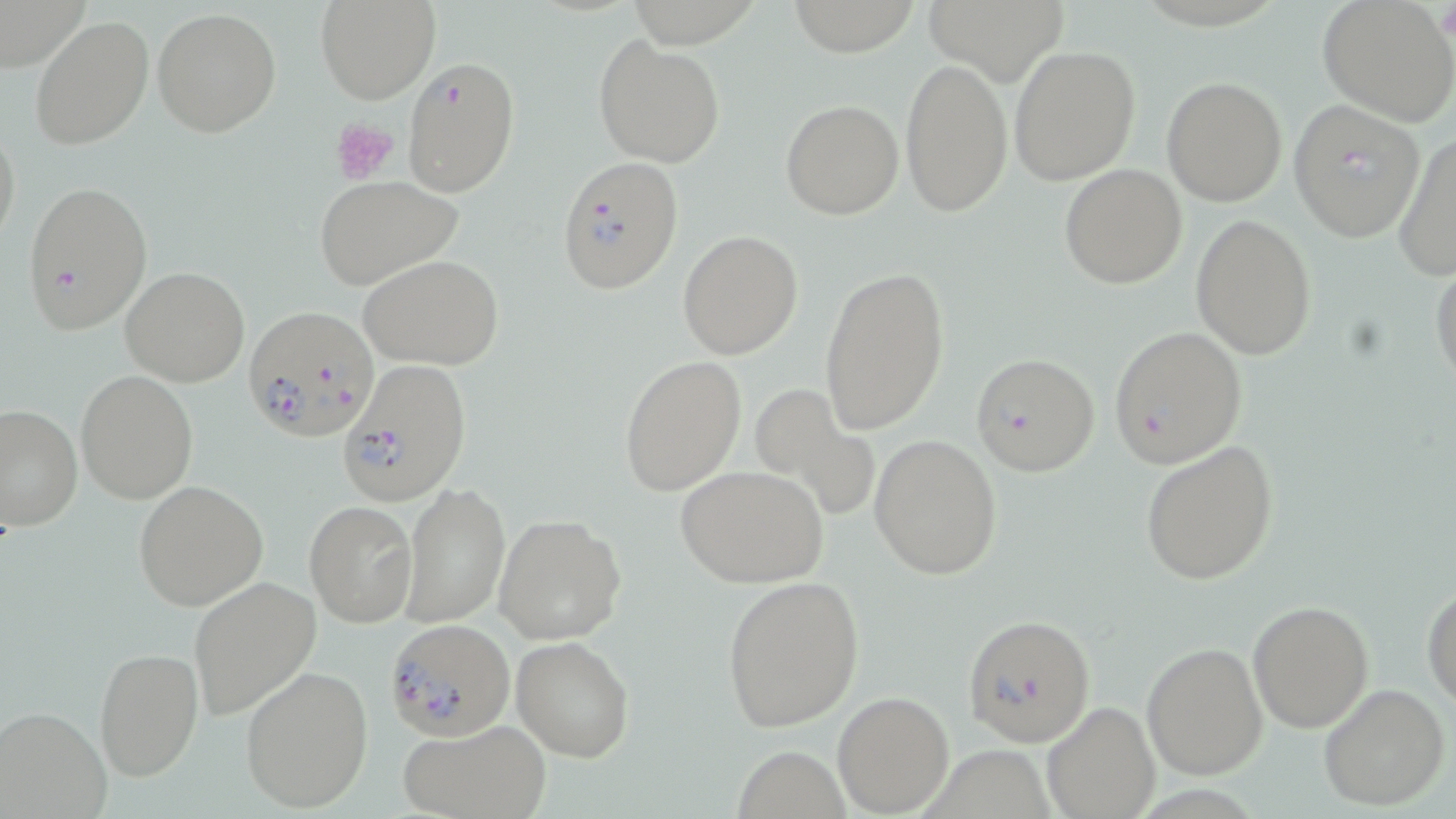
slide-level diagnosis = Plasmodium falciparum
image size = 1456×819 pixels
stain = May-Grünwald-Giemsa
modality = optical microscopy
magnification = 1000x
uninfected red blood cell locations = approximate bounding boxes as (x1,y1)-(x2,y2) corner pairs in pixels: (316,0)-(438,103), (785,0)-(924,56), (1317,1)-(1455,125), (151,7)-(281,139), (29,14)-(154,150), (594,35)-(725,167), (1008,45)-(1141,186), (900,57)-(1013,218), (1161,77)-(1288,206), (780,99)-(904,220), (0,121)-(21,253), (1392,129)-(1456,282), (1059,163)-(1187,289), (314,176)-(462,291), (1191,215)-(1316,361), (677,231)-(802,359), (359,254)-(504,370), (1430,259)-(1456,396), (819,265)-(951,435), (120,267)-(251,387), (620,355)-(746,496), (75,370)-(198,504), (748,383)-(878,523), (0,404)-(82,532), (869,434)-(1002,581), (1138,439)-(1280,585), (677,465)-(829,588), (134,480)-(269,611), (402,482)-(510,626), (304,500)-(417,627), (494,515)-(625,645), (188,574)-(322,723), (720,574)-(865,732), (1423,583)-(1456,710), (1247,599)-(1374,730), (512,635)-(635,760), (1141,641)-(1269,779), (93,645)-(204,782), (240,664)-(373,813), (1318,683)-(1449,811), (832,691)-(955,817), (1042,700)-(1159,819), (0,705)-(112,817), (397,720)-(551,819), (735,742)-(852,817)
platelet locations = approximate bounding boxes as (x1,y1)-(x2,y2) corner pairs in pixels: (1436,6)-(1456,43), (332,117)-(399,187)
Plasmodium falciparum-infected red blood cell locations = approximate bounding boxes as (x1,y1)-(x2,y2) corner pairs in pixels: (402,57)-(520,196), (1288,100)-(1428,240), (554,154)-(684,294), (22,179)-(153,335), (242,305)-(376,441), (1109,326)-(1248,470), (972,353)-(1100,477), (337,358)-(472,508), (962,613)-(1096,748), (388,620)-(513,739)
preparation = thin blood film
field of view = single